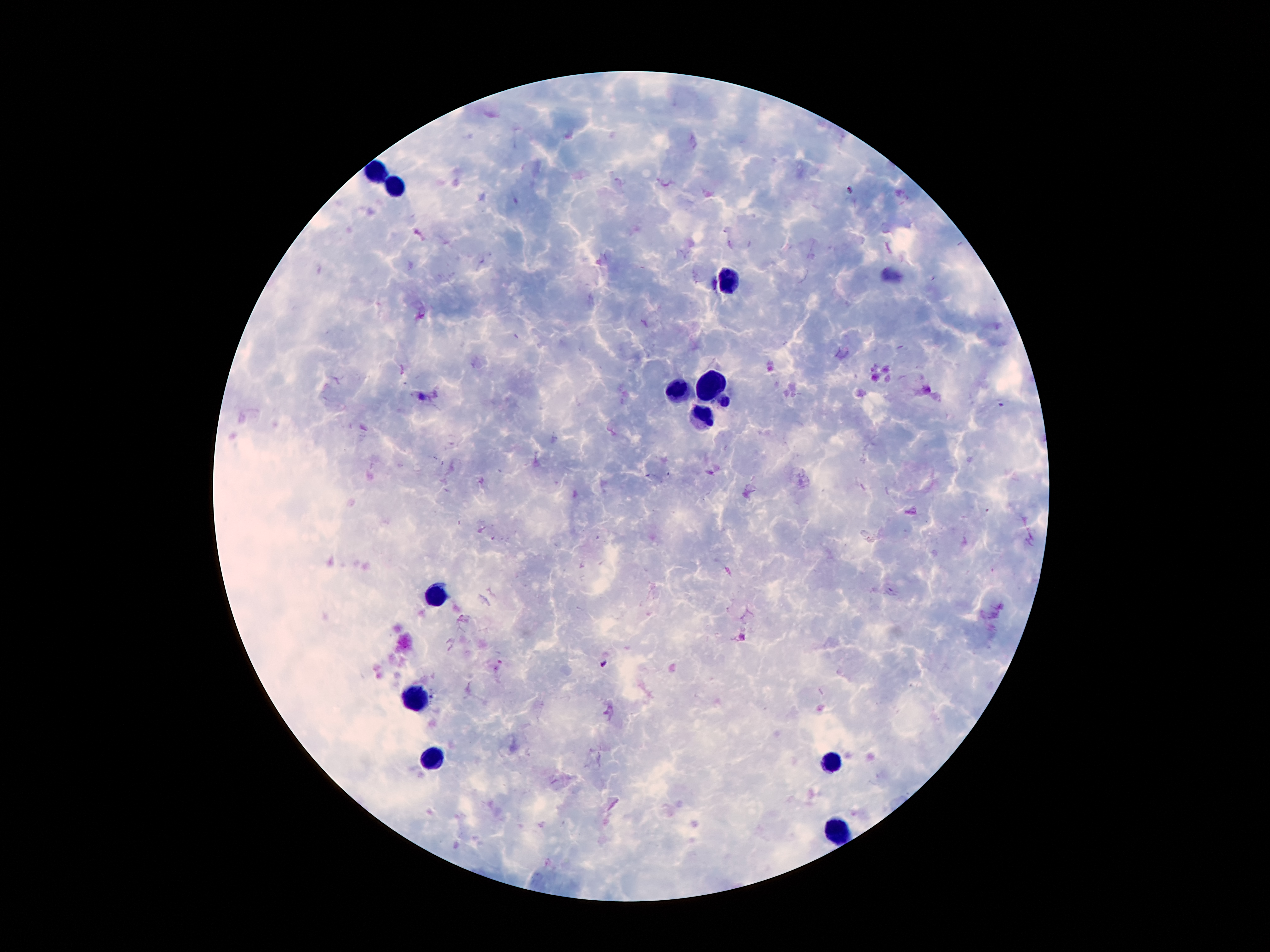
coordinate format = approximate object centers, in pixels from the top-left corner
leukocyte locations = (x=378, y=173), (x=396, y=186), (x=726, y=280), (x=712, y=384), (x=679, y=391), (x=700, y=415), (x=435, y=595), (x=419, y=698), (x=433, y=759), (x=833, y=761), (x=839, y=829)
malaria parasite locations = (x=852, y=189), (x=422, y=397), (x=605, y=664)
magnification = 100x
preparation = thick blood film
capture = smartphone camera through the microscope eyepiece
image size = 1270×952 pixels
patient malaria status = infected with Plasmodium falciparum
field of view = single
stain = Giemsa